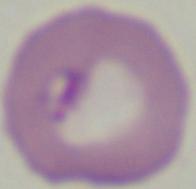

Photomicrograph. Captured at 1000x magnification. A Babesia parasite is seen.